Give the extent of all uninfected red blood cells.
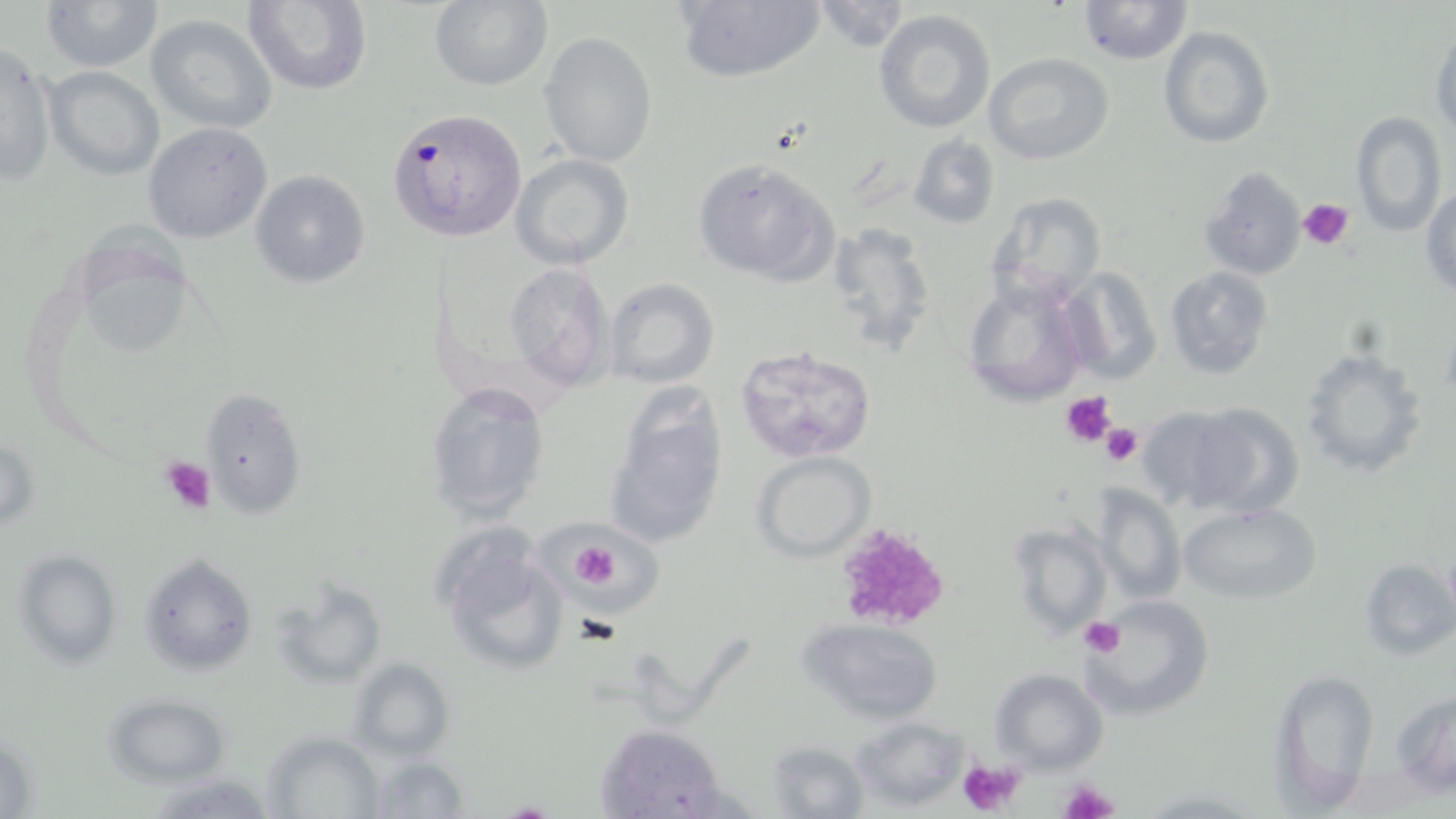

Approximate bounding boxes as named x1/y1/x2/y2 corners in pixels.
Uninfected red blood cells: (x1=244, y1=0, x2=371, y2=94), (x1=429, y1=0, x2=552, y2=90), (x1=675, y1=0, x2=825, y2=83), (x1=1078, y1=0, x2=1192, y2=65), (x1=42, y1=1, x2=162, y2=73), (x1=811, y1=1, x2=910, y2=52), (x1=873, y1=8, x2=996, y2=133), (x1=145, y1=13, x2=277, y2=133), (x1=1158, y1=26, x2=1273, y2=148), (x1=1430, y1=29, x2=1455, y2=136), (x1=539, y1=33, x2=658, y2=167), (x1=1, y1=42, x2=57, y2=187), (x1=983, y1=51, x2=1115, y2=165), (x1=45, y1=67, x2=165, y2=180), (x1=1350, y1=110, x2=1446, y2=236), (x1=143, y1=123, x2=272, y2=244), (x1=909, y1=134, x2=1000, y2=229), (x1=511, y1=154, x2=635, y2=271), (x1=693, y1=158, x2=840, y2=286), (x1=1198, y1=165, x2=1307, y2=282), (x1=250, y1=169, x2=371, y2=290), (x1=1422, y1=186, x2=1455, y2=296), (x1=983, y1=193, x2=1105, y2=308), (x1=827, y1=221, x2=937, y2=357), (x1=504, y1=260, x2=616, y2=395), (x1=1060, y1=265, x2=1163, y2=383), (x1=1165, y1=266, x2=1273, y2=380), (x1=604, y1=277, x2=721, y2=389), (x1=962, y1=278, x2=1087, y2=407), (x1=733, y1=345, x2=877, y2=463), (x1=1302, y1=345, x2=1427, y2=478), (x1=424, y1=382, x2=554, y2=523), (x1=603, y1=386, x2=732, y2=551), (x1=201, y1=391, x2=306, y2=519), (x1=1188, y1=401, x2=1305, y2=517), (x1=1133, y1=405, x2=1248, y2=511), (x1=1, y1=432, x2=39, y2=535), (x1=753, y1=451, x2=874, y2=559), (x1=1090, y1=482, x2=1187, y2=605), (x1=1178, y1=503, x2=1322, y2=605), (x1=539, y1=515, x2=667, y2=624), (x1=1008, y1=522, x2=1114, y2=641), (x1=436, y1=539, x2=569, y2=678), (x1=13, y1=549, x2=121, y2=668), (x1=139, y1=553, x2=258, y2=677), (x1=1358, y1=559, x2=1455, y2=659), (x1=274, y1=580, x2=388, y2=689), (x1=1086, y1=595, x2=1217, y2=720), (x1=798, y1=617, x2=943, y2=724), (x1=349, y1=657, x2=453, y2=762), (x1=1272, y1=666, x2=1379, y2=808), (x1=991, y1=670, x2=1108, y2=773), (x1=1391, y1=692, x2=1455, y2=797), (x1=104, y1=693, x2=229, y2=785), (x1=849, y1=716, x2=970, y2=810), (x1=601, y1=724, x2=728, y2=817), (x1=263, y1=731, x2=383, y2=817), (x1=766, y1=741, x2=869, y2=818), (x1=368, y1=756, x2=471, y2=817), (x1=145, y1=771, x2=272, y2=817).

{
  "slide_level_diagnosis": "Plasmodium falciparum",
  "stain": "May-Grünwald-Giemsa",
  "magnification": "1000x",
  "plasmodium_falciparum_infected_red_blood_cell_locations": "approximate bounding boxes as named x1/y1/x2/y2 corners in pixels: (x1=389, y1=107, x2=531, y2=244)",
  "image_size": "1456×819 pixels",
  "platelet_locations": "approximate bounding boxes as named x1/y1/x2/y2 corners in pixels: (x1=1298, y1=197, x2=1353, y2=250), (x1=1059, y1=390, x2=1118, y2=450), (x1=1100, y1=420, x2=1145, y2=468), (x1=157, y1=455, x2=216, y2=516), (x1=833, y1=524, x2=950, y2=631), (x1=571, y1=540, x2=619, y2=588), (x1=1080, y1=617, x2=1125, y2=658), (x1=958, y1=758, x2=1027, y2=816), (x1=1059, y1=779, x2=1119, y2=819)",
  "modality": "optical microscopy",
  "field_of_view": "one of a larger specimen",
  "preparation": "thin blood film"
}